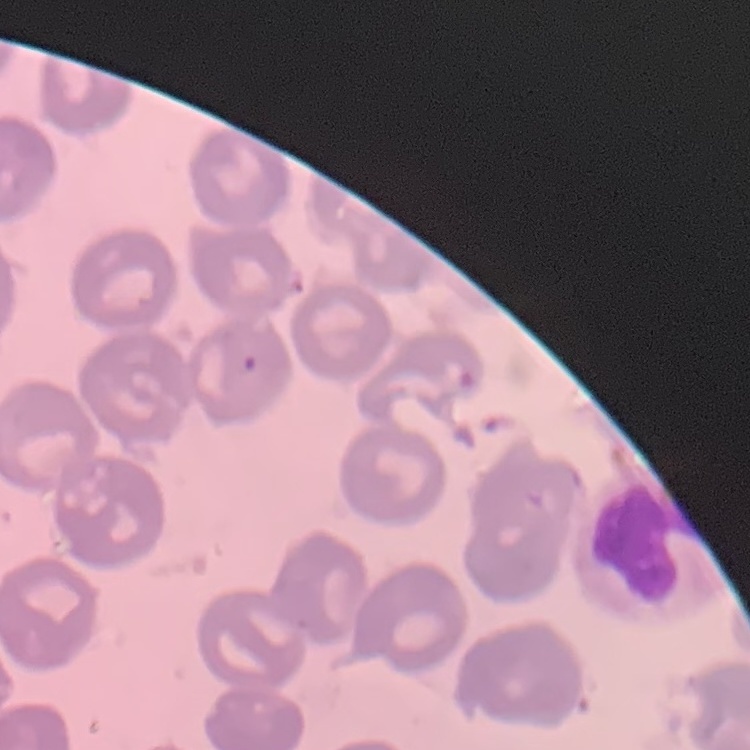
erythrocyte morphology = no rouleaux formation
preparation = thin blood film
stain = Field's or Giemsa
image type = one tile cut from a larger photomicrograph